Describe the morphology of the red blood cells.
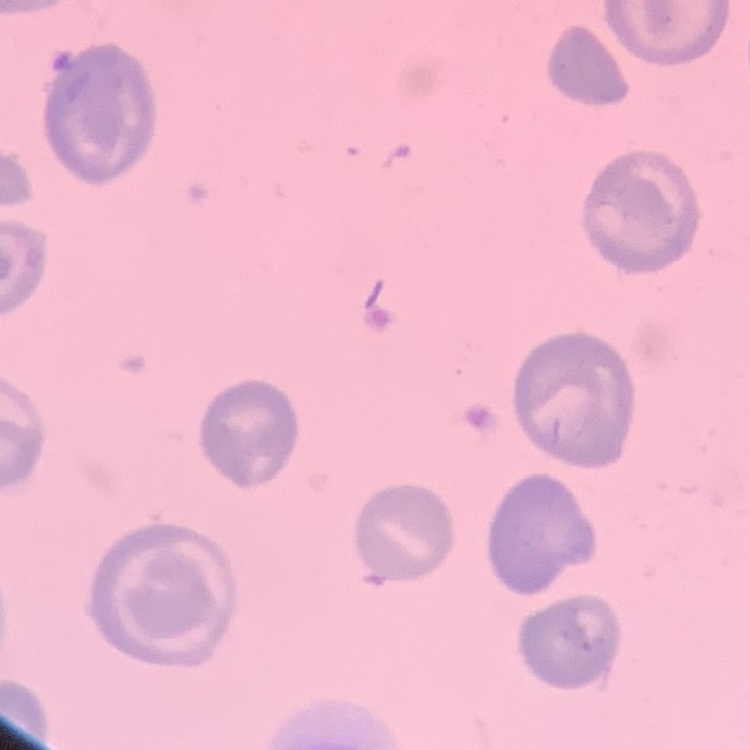
They show no rouleaux formation.

Stained with either Field's or Giemsa. Thin blood film. Square crop of a larger photomicrograph.